Report the malaria status of this cell.
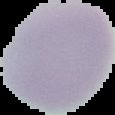
Uninfected.

{
  "image_type": "cell region segmented out of the field of view; surrounding area masked to black",
  "image_size": "115×115 pixels",
  "preparation": "thin blood film"
}